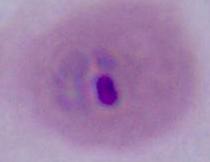

Summary:
  - Magnification: 400x or 1000x
  - Modality: photomicrograph
  - Identification: Plasmodium